Classify this cell by malaria status.
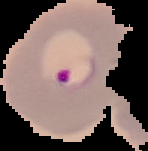

It is parasitized.

Summary:
  - Image type: segmented cell region on a black background
  - Preparation: thin blood smear
  - Image size: 148×151 pixels